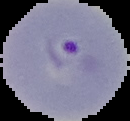

From a thin blood film. Image is 130×121 pixels. Result: malaria parasites identified. Cell region segmented out of the field of view; the surrounding area is masked to black.